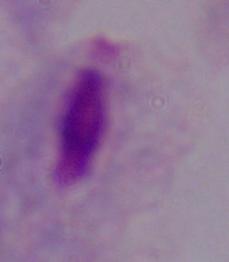

Summary:
  - Identification: trichomonad
  - Modality: micrograph
  - Magnification: 1000x